Report the malaria status of this cell.
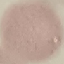

Uninfected.

capture: smartphone camera at the microscope eyepiece
stain: Giemsa
image_type: cell patch, automatically extracted from a larger field of view and resized to 64 × 64 pixels
preparation: thin blood film